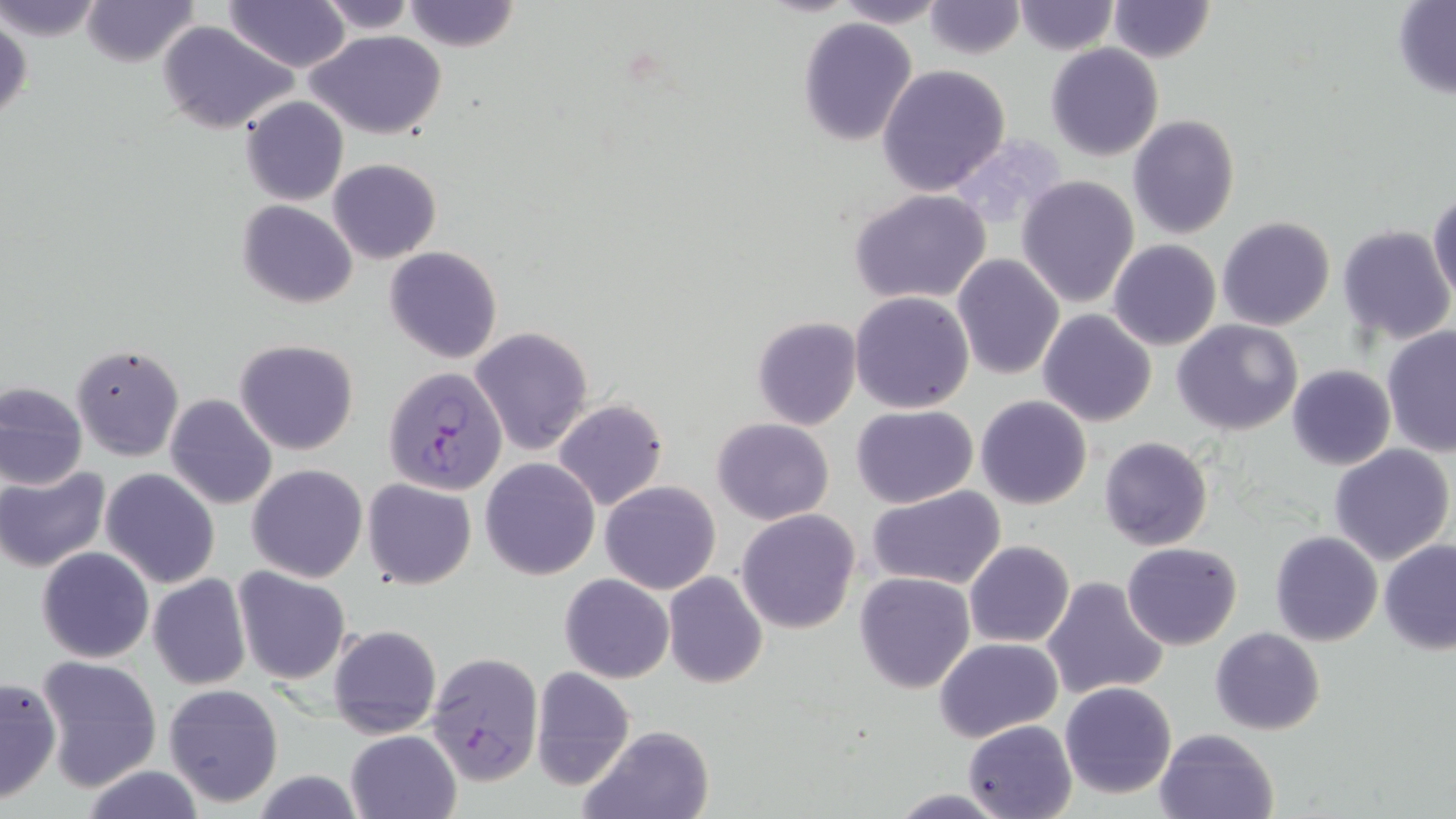

Approximate bounding boxes as [x1, y1, x2, y2] in pixels. Uninfected red blood cell locations: [0, 0, 107, 45], [78, 0, 199, 67], [223, 0, 351, 70], [313, 0, 419, 34], [402, 0, 521, 53], [836, 0, 946, 27], [1104, 0, 1214, 62], [922, 1, 1026, 58], [1012, 1, 1119, 54], [1393, 2, 1456, 98], [1, 12, 32, 132], [797, 18, 918, 145], [156, 21, 299, 135], [306, 30, 447, 139], [1045, 44, 1164, 162], [877, 65, 1010, 197], [240, 95, 350, 205], [1128, 115, 1241, 240], [327, 157, 441, 264], [1017, 176, 1139, 308], [849, 189, 992, 307], [1428, 190, 1456, 301], [237, 199, 359, 308], [1217, 217, 1335, 331], [1336, 225, 1454, 346], [1107, 240, 1220, 351], [385, 246, 503, 365], [952, 254, 1065, 379], [849, 291, 974, 413], [1038, 309, 1158, 427], [752, 317, 862, 430], [1175, 319, 1301, 435], [470, 326, 594, 456], [1381, 326, 1456, 456], [234, 339, 359, 455], [71, 342, 185, 463], [1287, 364, 1395, 470], [0, 380, 89, 492], [166, 393, 277, 509], [975, 395, 1091, 509], [553, 398, 668, 509], [851, 405, 979, 509], [712, 417, 833, 524], [1099, 436, 1213, 551], [1330, 445, 1454, 565], [481, 458, 600, 580], [247, 463, 369, 582], [0, 466, 110, 572], [99, 467, 220, 588], [362, 478, 477, 590], [600, 480, 721, 595], [867, 485, 1007, 590], [735, 509, 861, 634], [1269, 531, 1381, 646], [1378, 539, 1456, 654], [964, 541, 1074, 648], [1122, 541, 1242, 649], [36, 547, 155, 664], [233, 567, 352, 685], [663, 571, 767, 688], [854, 571, 975, 694], [147, 572, 251, 690], [560, 573, 673, 683], [1041, 575, 1168, 702], [327, 624, 442, 739], [1210, 626, 1326, 735], [936, 637, 1061, 742], [35, 655, 161, 791], [531, 665, 635, 789], [0, 677, 59, 803], [1061, 681, 1178, 800], [162, 682, 285, 808], [962, 719, 1078, 818], [579, 725, 716, 819], [1154, 728, 1279, 819], [346, 730, 462, 819], [886, 788, 1020, 818]. Plasmodium falciparum-infected red blood cell locations: [383, 367, 508, 496], [428, 650, 545, 784]. Slide-level diagnosis: Plasmodium falciparum. Thin blood smear. 1000x magnification. Image is 1456×819 pixels. May-Grünwald-Giemsa stain. Optical microscopy. Single field of view.